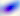
magnification = 400x
modality = photomicrograph
identification = Toxoplasma gondii